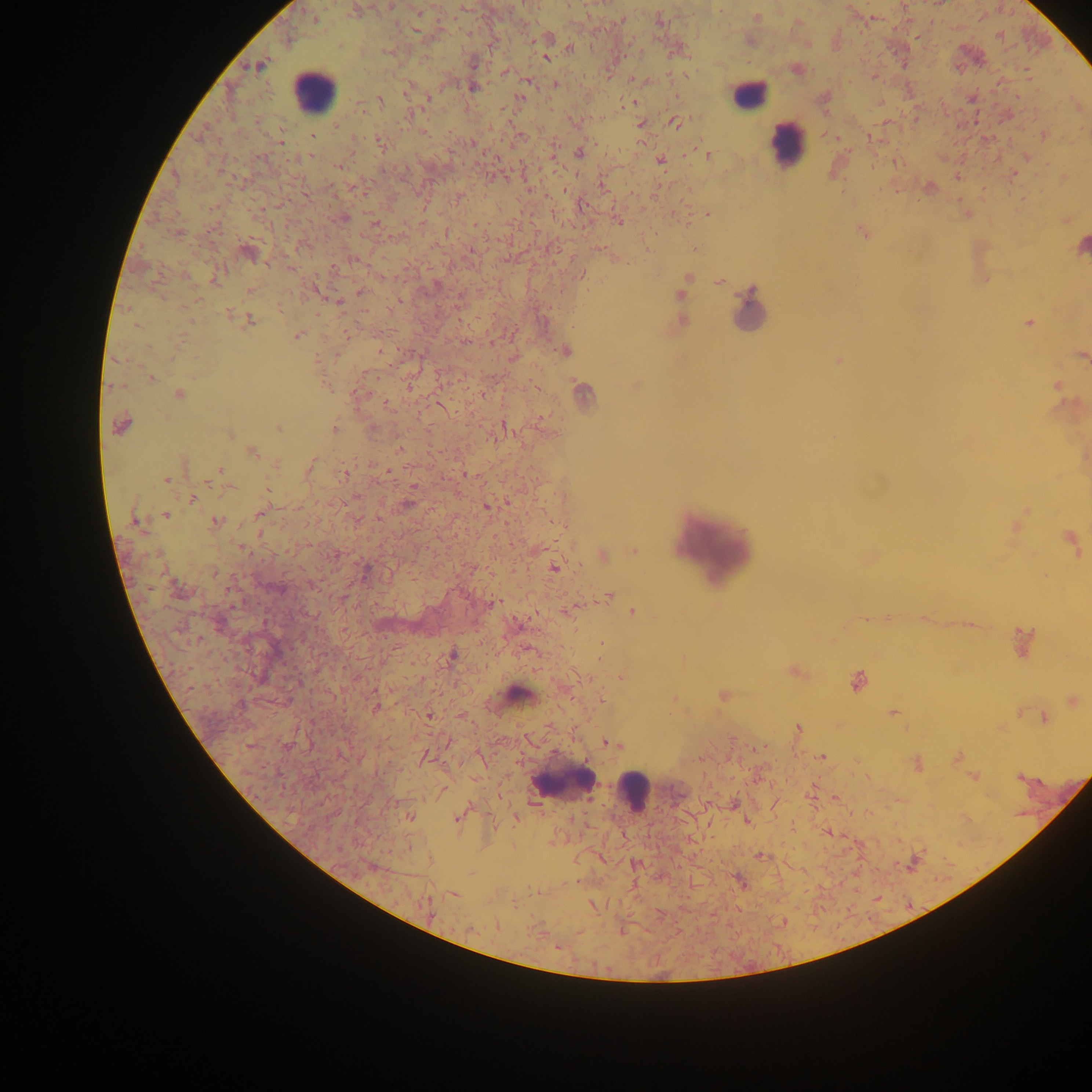
leukocyte locations = approximate centers as x y in pixels: 311 90; 748 96; 786 143; 750 309; 713 550; 519 696; 564 781; 632 791
preparation = thick blood film
capture = mobile-phone photograph through a microscope
image size = 1092×1092 pixels
object labeled both malaria parasite and leukocyte by the source = approximate centers as x y in pixels: 1081 244
country = Ghana
field of view = single
malaria parasite locations = approximate centers as x y in pixels: 390 6; 356 10; 756 17; 314 18; 872 18; 621 19; 659 19; 998 36; 545 37; 917 37; 749 40; 570 48; 388 51; 546 57; 257 65; 796 69; 506 72; 874 77; 528 80; 555 85; 408 87; 472 87; 520 97; 972 98; 427 99; 824 99; 379 100; 632 103; 1078 106; 675 122; 640 124; 1043 134; 835 137; 869 138; 280 139; 381 145; 579 152; 707 154; 1026 157; 659 160; 894 162; 338 165; 957 175; 1013 175; 602 185; 928 187; 564 189; 457 198; 580 206; 707 214; 966 214; 342 218; 1066 219; 618 221; 374 223; 474 224; 862 232; 177 234; 393 237; 695 249; 470 250; 248 252; 614 257; 290 268; 581 274; 215 277; 985 279; 685 281; 719 281; 316 290; 250 291; 361 291; 682 293; 339 302; 680 306; 248 320; 681 320; 1029 323; 296 335; 347 335; 464 342; 564 350; 379 351; 1081 355; 514 357; 839 360; 151 377; 636 384; 410 385; 535 386; 1057 386; 581 392; 359 393; 178 394; 482 394; 387 404; 121 424; 504 426; 278 427; 334 429; 229 433; 401 450; 251 452; 311 466; 219 471; 346 471; 469 474; 166 479; 229 486; 267 489; 191 499; 408 502; 486 507; 260 513; 164 515; 136 521; 215 521; 1019 525; 1071 542; 635 551; 602 556; 870 556; 554 567; 178 589; 608 596; 492 603; 567 610; 633 611; 924 618; 867 619; 1024 642; 601 644; 450 655; 795 671; 621 677; 856 681; 723 695; 601 699; 674 700; 1072 700; 375 706; 893 712; 1019 712; 428 715; 1043 718; 798 728; 448 741; 610 743; 760 747; 424 756; 821 757; 957 757; 916 763; 1018 776; 973 777; 835 797; 460 815; 408 816; 515 816; 746 820; 827 832; 760 856; 635 865; 741 883; 454 893; 427 905; 592 905